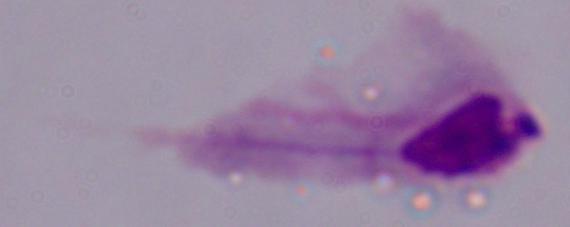
{
  "identification": "trichomonad",
  "modality": "micrograph",
  "magnification": "1000x"
}